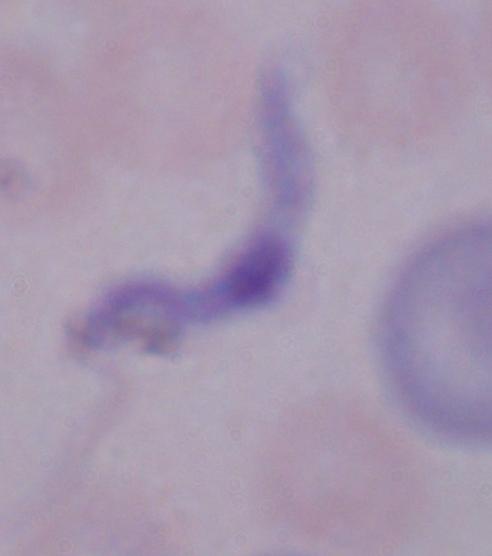
Summary:
  - Identification: trypanosome
  - Modality: photomicrograph
  - Magnification: 1000x